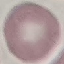

Summary:
  - Malaria status: uninfected
  - Preparation: thin blood smear
  - Image type: automatically extracted cell patch, resized to 64 × 64 pixels
  - Stain: Giemsa
  - Capture: smartphone camera at the microscope eyepiece